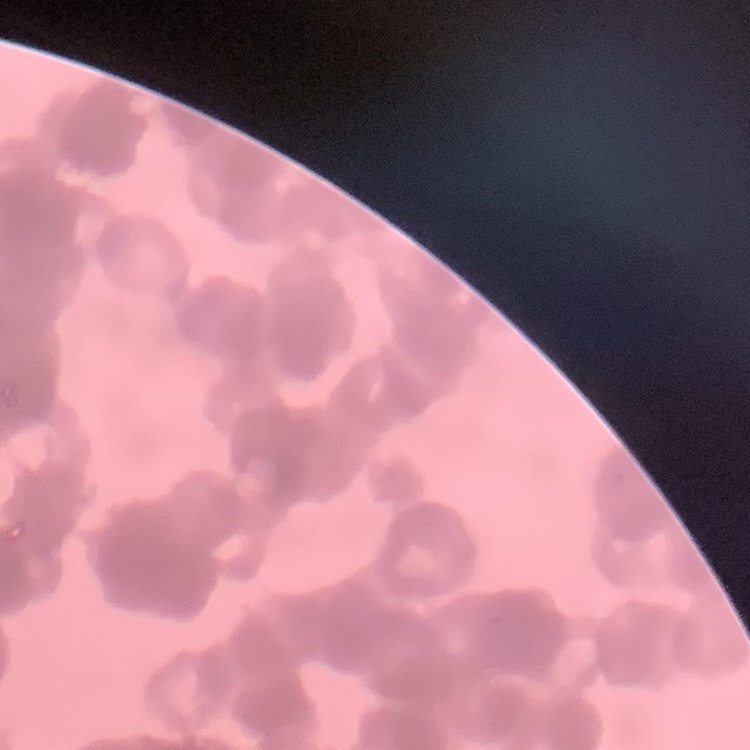
Summary:
  - Erythrocyte morphology: rouleaux formation
  - Preparation: thin blood smear
  - Stain: Field's or Giemsa
  - Image type: one tile cut from a larger photomicrograph